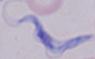

modality = photomicrograph
magnification = 1000x
identification = trypanosome